Classify this cell by malaria status.
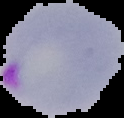

It is parasitized.

Summary:
  - Image type: segmented cell region on a black background
  - Preparation: thin blood film
  - Image size: 124×118 pixels